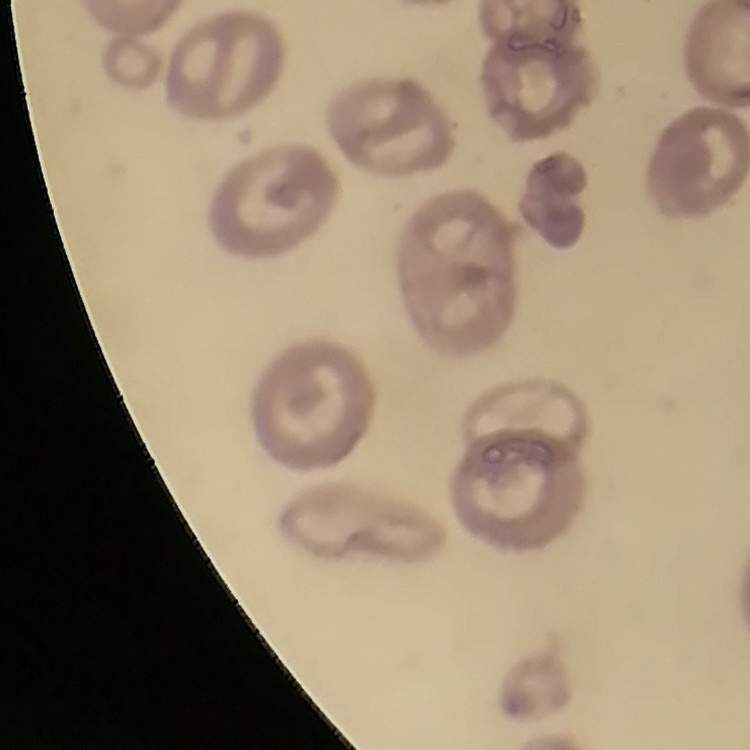

{
  "erythrocyte_morphology": "no rouleaux formation",
  "preparation": "thin blood smear",
  "image_type": "square crop of a larger photomicrograph",
  "stain": "Field's or Giemsa"
}